Assess this cell for malaria.
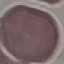
Uninfected.

Thin blood smear. Automatically extracted cell patch, resized to 64 × 64 pixels. Giemsa-stained preparation. Photographed with a smartphone camera at the microscope eyepiece.